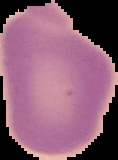

Summary:
  - Preparation: thin blood film
  - Image size: 118×160 pixels
  - Result: no malaria parasites detected
  - Image type: segmented cell region on a black background